Classify this cell by malaria status.
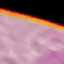

Uninfected.

image type = automatically extracted cell patch, resized to 64 × 64 pixels
stain = Giemsa
capture = smartphone camera at the microscope eyepiece
preparation = thin smear